Report the malaria status of this cell.
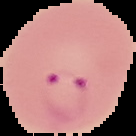
Parasitized.

From a thin blood film. Cell region segmented out of the field of view; the surrounding area is masked to black. Image is 136×136 pixels.